Report the malaria status of this cell.
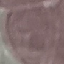

Uninfected.

Photographed with a smartphone camera at the microscope eyepiece. Thin blood smear. Giemsa stain. Automatically extracted cell patch, resized to 64 × 64 pixels.